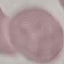
{
  "malaria_status": "uninfected",
  "preparation": "thin blood film",
  "image_type": "cell patch, automatically extracted from a larger field of view and resized to 64 × 64 pixels",
  "stain": "Giemsa",
  "capture": "smartphone through the microscope eyepiece"
}